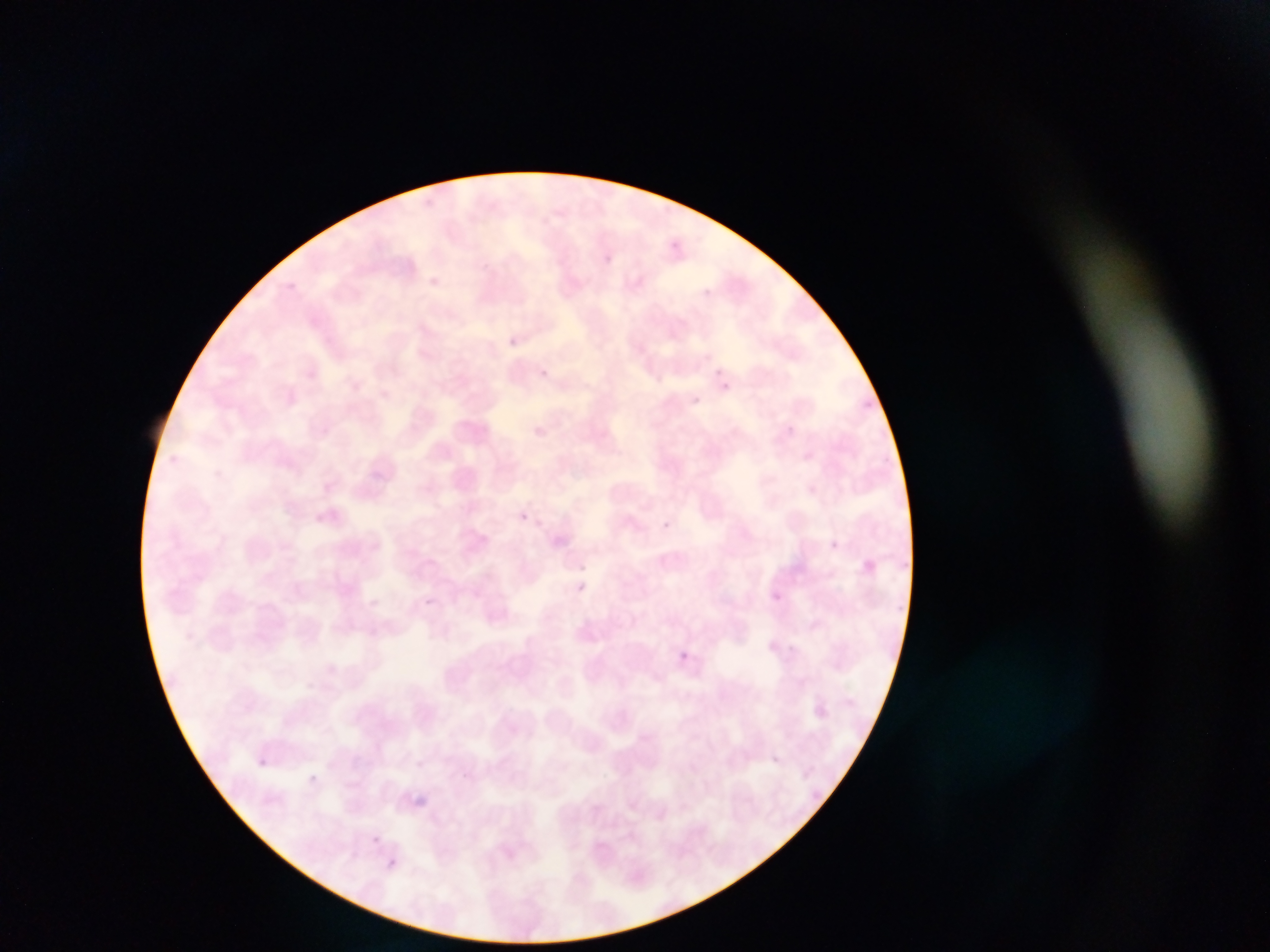
Approximate bounding boxes as [left, top, right, bottom] in pixels. Malaria parasite locations: [508, 337, 519, 347], [539, 368, 549, 378], [716, 368, 724, 377], [721, 383, 729, 391], [692, 396, 701, 404], [520, 512, 529, 522], [659, 520, 672, 535], [826, 541, 845, 559], [575, 580, 591, 594], [774, 590, 782, 602], [679, 650, 690, 664], [257, 759, 267, 768], [308, 774, 318, 783], [416, 796, 428, 806], [371, 835, 381, 844]. Thin blood smear. Photographed through a microscope with a mobile-phone camera. Collected in Ghana. One field of view. Image is 1270×952 pixels.